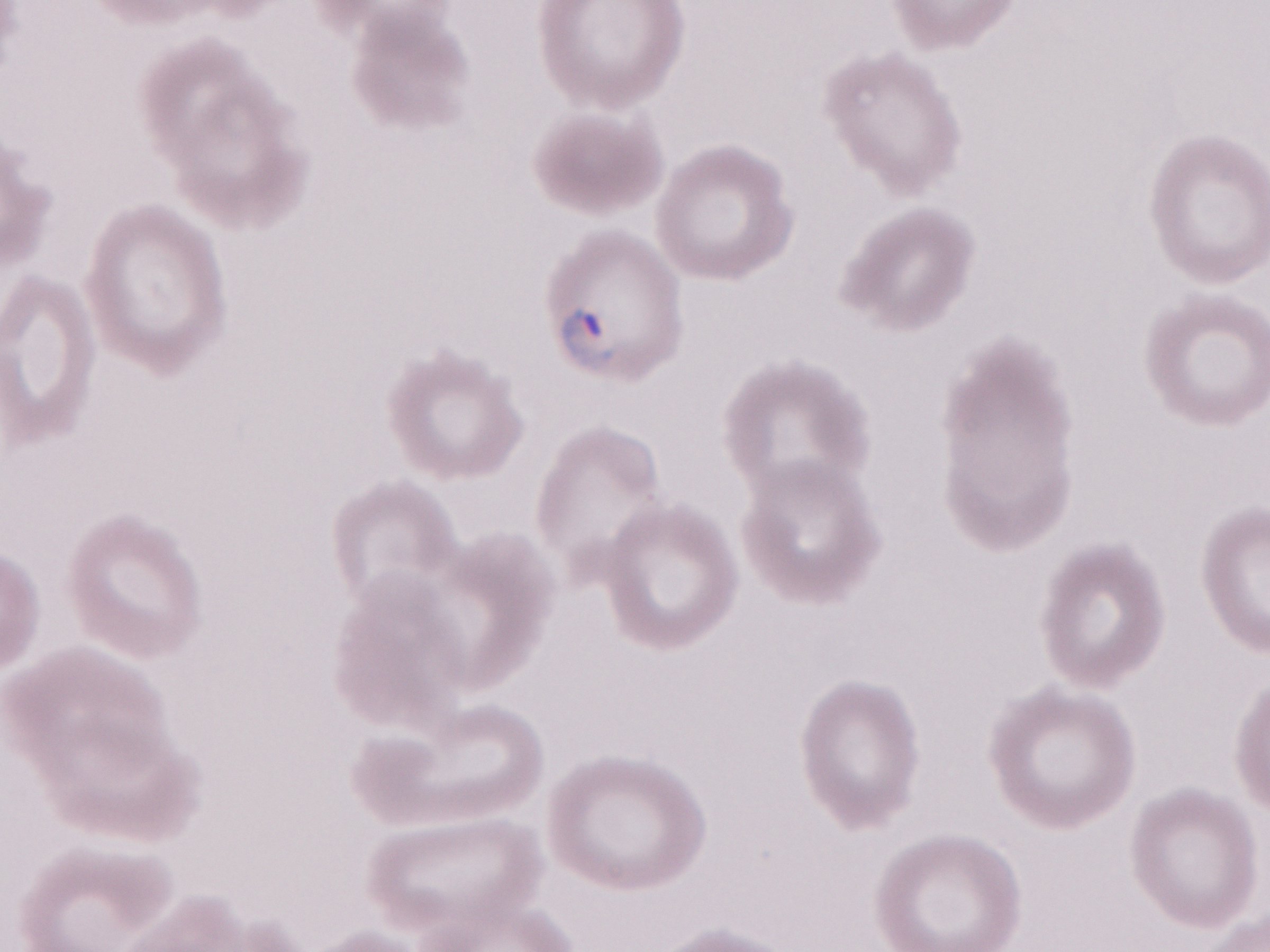 Thin peripheral-blood smear. May-Grünwald-Giemsa (MGG) stain. Olympus BX43 microscope and DP73 digital camera. Patient-level malaria diagnosis: positive. 1,000x magnification. One field of this slide. Image is 1270×952 pixels.